Locate every uninfected red blood cell.
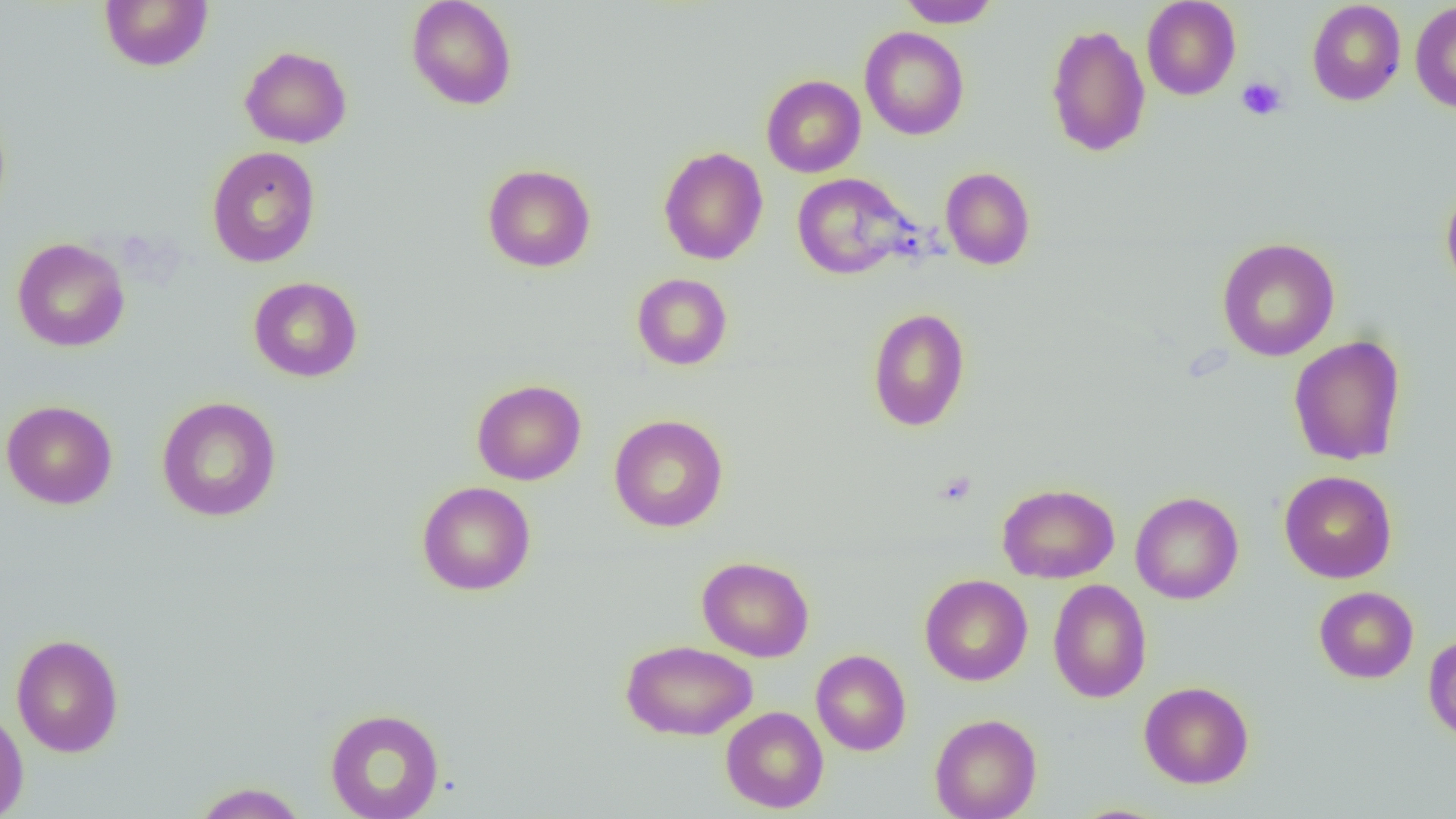

Approximate bounding boxes as [x1, y1, x2, y2] in pixels.
Uninfected red blood cells: [99, 0, 213, 71], [406, 0, 517, 110], [897, 0, 1000, 28], [1142, 0, 1241, 100], [1306, 1, 1406, 105], [1410, 2, 1456, 114], [1046, 24, 1151, 158], [859, 26, 969, 140], [240, 46, 352, 148], [761, 75, 865, 177], [206, 145, 321, 268], [658, 146, 768, 265], [482, 164, 596, 272], [940, 167, 1035, 270], [791, 173, 914, 279], [1441, 184, 1456, 294], [11, 237, 130, 352], [1216, 237, 1340, 361], [632, 273, 732, 370], [248, 276, 363, 382], [867, 307, 970, 432], [1288, 335, 1406, 466], [471, 379, 586, 485], [156, 396, 282, 522], [1, 400, 118, 509], [609, 414, 729, 533], [1279, 470, 1397, 583], [417, 481, 536, 596], [997, 483, 1120, 583], [1130, 491, 1244, 604], [697, 556, 814, 662], [919, 574, 1033, 686], [1048, 579, 1152, 703], [1314, 586, 1418, 683], [1423, 632, 1456, 742], [11, 633, 124, 758], [621, 639, 757, 740], [811, 649, 911, 756], [1139, 681, 1254, 788], [0, 706, 29, 819], [720, 707, 829, 813], [324, 708, 445, 818], [930, 713, 1042, 819], [191, 782, 308, 819].

slide-level diagnosis = negative for blood parasites
platelet locations = approximate bounding boxes as [x1, y1, x2, y2] in pixels: [1236, 76, 1287, 121]
image size = 1456×819 pixels
field of view = one of a larger specimen
modality = optical microscopy
preparation = thin blood smear
magnification = 1000x